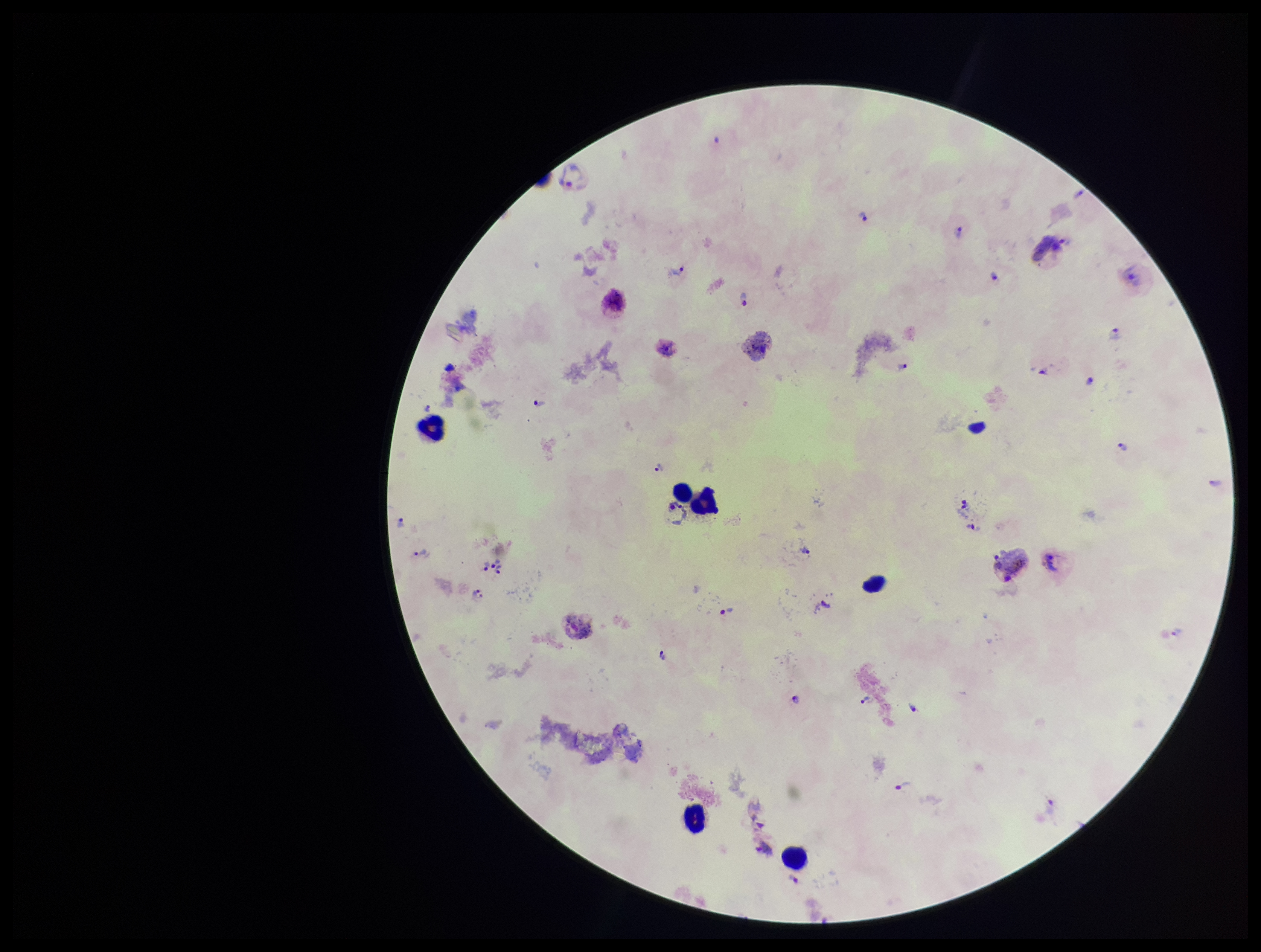

Photographed through the microscope eyepiece with a smartphone camera. Preparation: thick. Species reported for this patient: Plasmodium vivax. Patient malaria status: positive. Image is 1261×952 pixels. Plasmodium parasites: detected. Stained with Giemsa. Leukocyte count: 6. Parasite count: 21. Single field of view.